Report the malaria status of this cell.
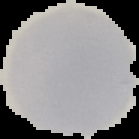

It is uninfected.

image type = segmented cell region with the area outside set to black
preparation = thin blood smear
image size = 139×139 pixels